Report the malaria status of this cell.
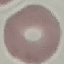
It is uninfected.

Cell patch, automatically extracted from a larger field of view and resized to 64 × 64 pixels. Giemsa stain. Acquired by smartphone through the microscope eyepiece. Thin blood smear.